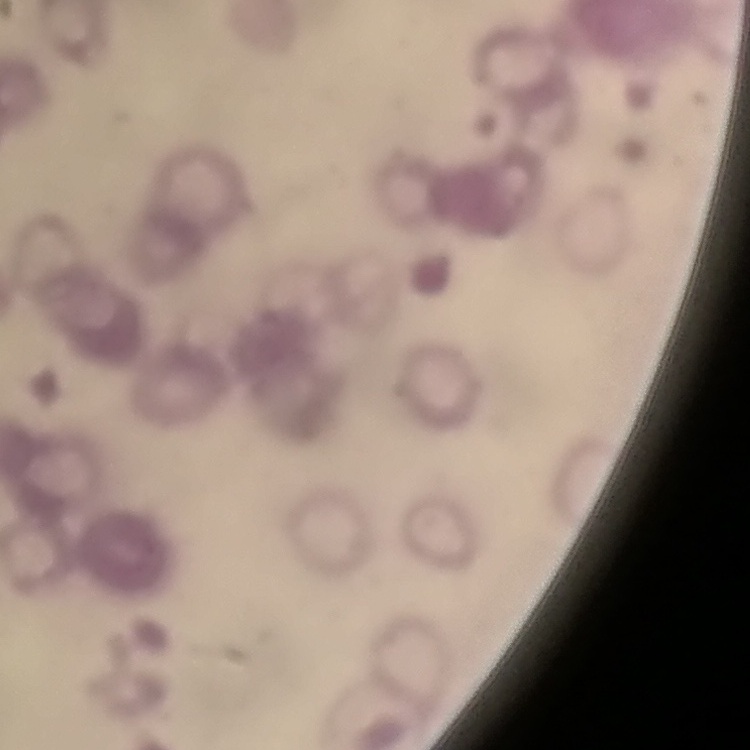

Summary:
  - Red blood cell morphology: rouleaux formation
  - Stain: Field's or Giemsa
  - Preparation: thin peripheral smear
  - Image type: one tile cut from a larger photomicrograph